Name the parasite shown.
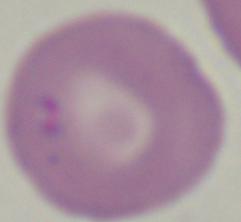

Babesia.

Summary:
  - Modality: photomicrograph
  - Magnification: 1000x